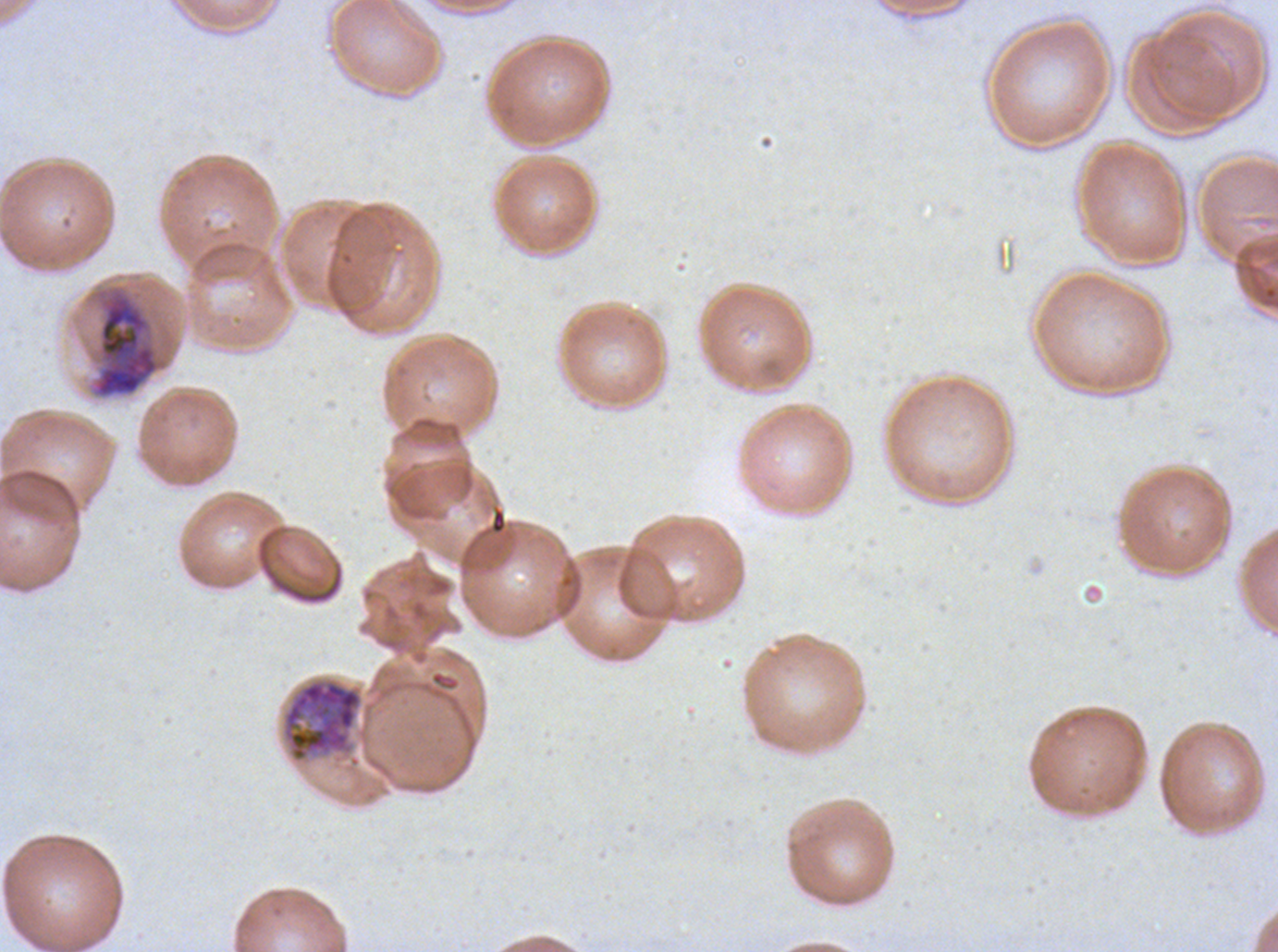
notation = approximate bounding boxes as (x1, y1, x2, y2) in pixels
late schizont locations = (92, 289, 161, 398), (281, 678, 363, 763)
field of view = one sub-image of a larger composite
stain = Giemsa
specimen = P. falciparum cultured ex vivo for 24 to 48 hours, from a patient in The Gambia
preparation = thin blood film
image size = 1278×952 pixels